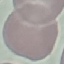
Summary:
  - Result: negative for malaria parasites
  - Image type: automatically extracted cell patch, resized to 64 × 64 pixels
  - Stain: Giemsa
  - Capture: smartphone camera at the microscope eyepiece
  - Preparation: thin blood smear